Report the malaria status of this cell.
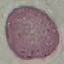

It is uninfected.

Acquired by smartphone through the microscope eyepiece. Thin smear of blood. Giemsa-stained preparation. Automatically extracted cell patch, resized to 64 × 64 pixels.